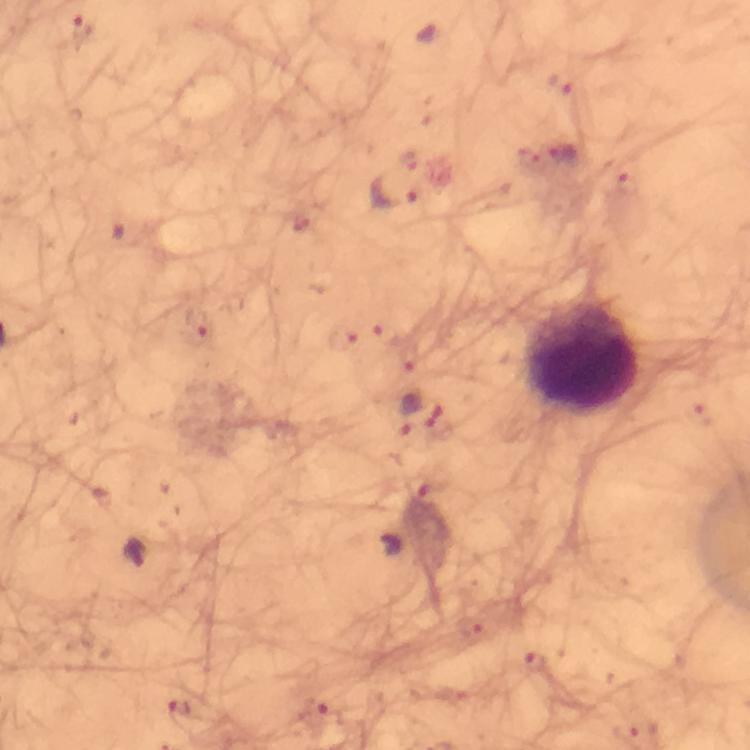

Plasmodium parasite locations = approximate centers as (x, y) in pixels: (83, 29), (561, 83), (565, 154), (391, 193), (199, 323), (410, 413), (390, 544), (138, 553), (534, 661), (181, 705)
image size = 750×750 pixels
leukocyte locations = approximate centers as (x, y) in pixels: (580, 353)
cropped from = a single field of view
context = from a diagnostic examination for malaria
magnification = 100x
immersion oil = applied
preparation = thick smear
stain = Giemsa
capture = smartphone photograph through a microscope